Report the malaria status of this cell.
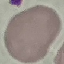

Uninfected.

{
  "capture": "smartphone through the microscope eyepiece",
  "preparation": "thin smear",
  "image_type": "cell patch, automatically extracted from a larger field of view and resized to 64 × 64 pixels",
  "stain": "Giemsa"
}